Assess the morphology of the red blood cells.
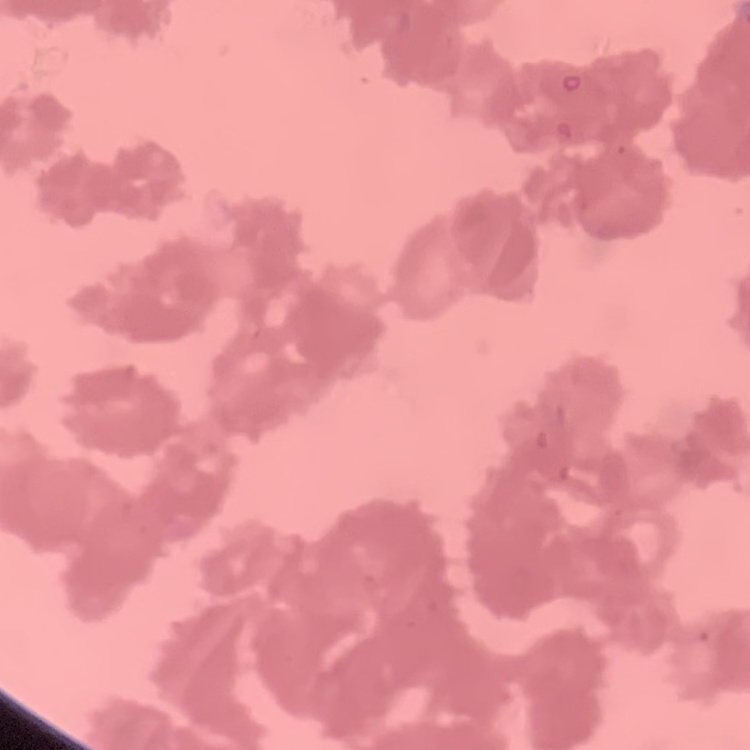
They show rouleaux formation.

Field's or Giemsa stain. Thin blood film. Square crop of a larger photomicrograph.